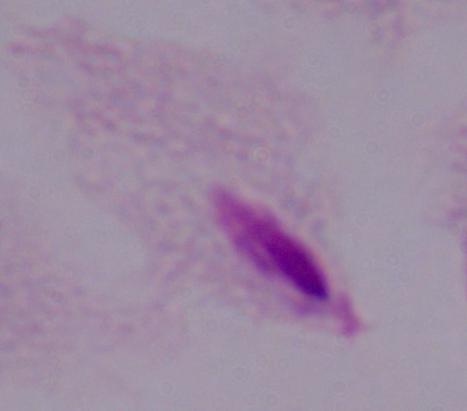

Summary:
  - Modality: micrograph
  - Magnification: 1000x
  - Identification: trichomonad